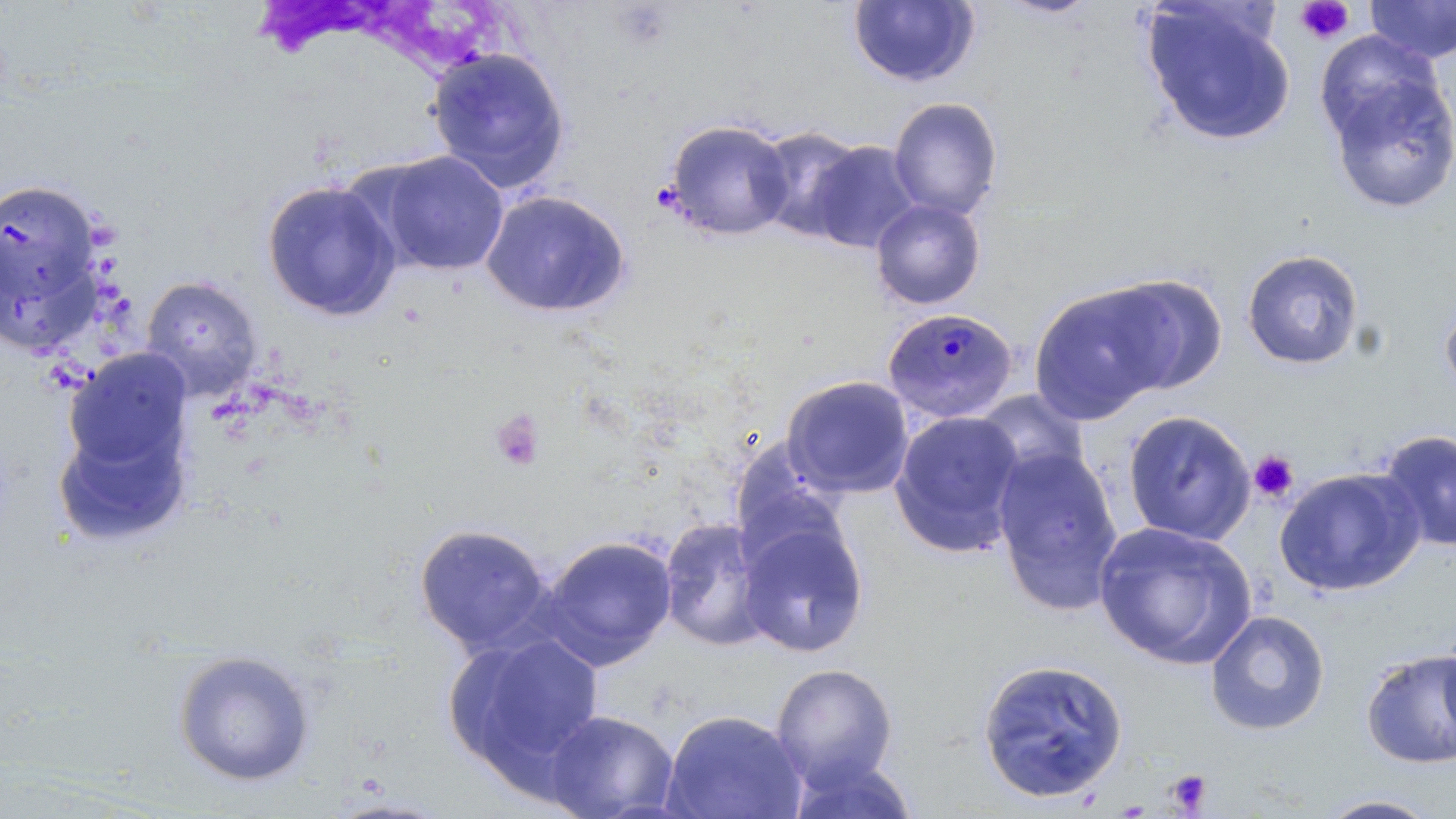

slide-level diagnosis = Plasmodium malariae
preparation = thin blood film
image size = 1456×819 pixels
magnification = 1000x
platelet locations = approximate bounding boxes as [x1, y1, x2, y2] in pixels: [1295, 1, 1354, 45], [490, 408, 546, 472], [1248, 451, 1300, 503], [1166, 768, 1213, 815]
field of view = one of a larger specimen
uninfected red blood cell locations = approximate bounding boxes as [x1, y1, x2, y2] in pixels: [1364, 0, 1456, 64], [847, 1, 980, 88], [1141, 1, 1296, 147], [427, 47, 570, 193], [1325, 69, 1456, 215], [887, 97, 1003, 220], [663, 119, 795, 241], [752, 126, 871, 242], [806, 140, 922, 253], [372, 150, 509, 277], [0, 176, 106, 339], [262, 179, 402, 322], [480, 189, 631, 318], [870, 199, 987, 310], [1241, 249, 1365, 370], [1100, 273, 1228, 394], [141, 275, 263, 401], [1028, 282, 1173, 424], [1439, 293, 1456, 404], [63, 348, 193, 480], [781, 375, 915, 500], [971, 388, 1090, 491], [889, 410, 1026, 558], [1122, 410, 1256, 545], [51, 415, 191, 548], [1377, 429, 1456, 552], [727, 438, 849, 559], [991, 446, 1124, 615], [1273, 466, 1425, 596], [736, 515, 870, 658], [658, 516, 773, 652], [1092, 521, 1258, 669], [414, 522, 553, 655], [538, 534, 678, 670], [1205, 609, 1330, 736], [1436, 624, 1456, 757], [444, 631, 605, 785], [1360, 648, 1456, 770], [172, 650, 316, 786], [976, 657, 1129, 803], [770, 662, 898, 791], [660, 708, 808, 819], [544, 709, 679, 819], [784, 754, 920, 819], [1312, 793, 1446, 818]
modality = optical microscopy
stain = May-Grünwald-Giemsa
Plasmodium malariae-infected red blood cell locations = approximate bounding boxes as [x1, y1, x2, y2] in pixels: [883, 306, 1019, 423]